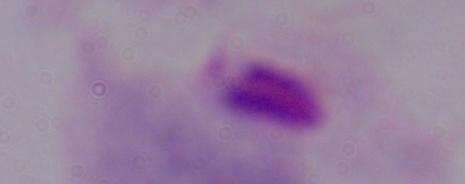

{
  "modality": "micrograph",
  "identification": "trichomonad",
  "magnification": "1000x"
}